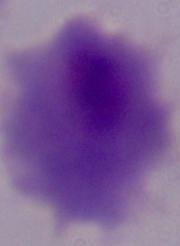 A trichomonad is seen. Captured at 1000x magnification. Micrograph.